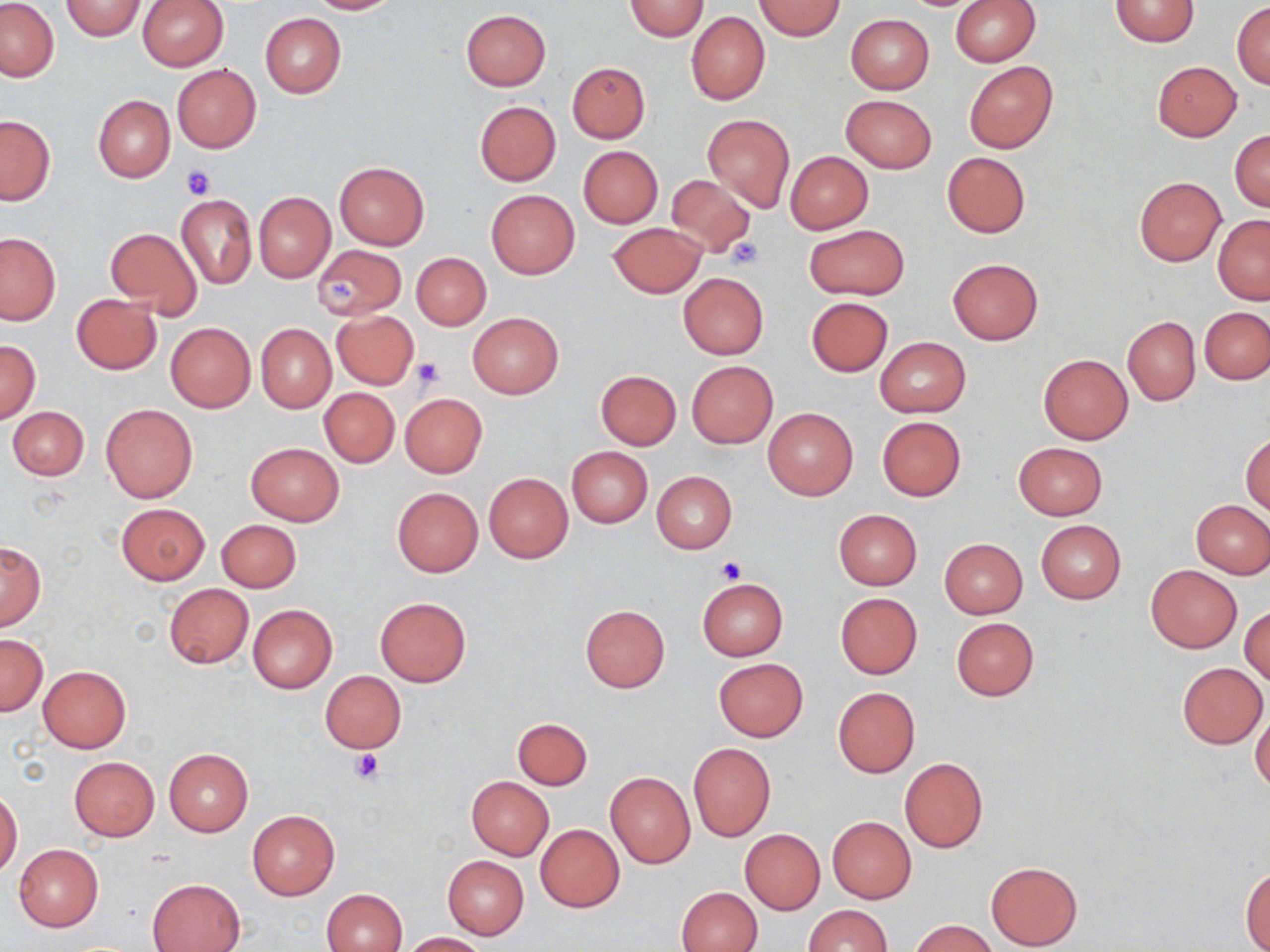

slide_level_diagnosis: no evidence of blood parasites
preparation: thin blood smear
stain: May-Grünwald-Giemsa
platelet_locations: 'approximate bounding boxes as (x1, y1, x2, y2) in pixels: (181, 165, 216, 200), (725, 237, 766, 269), (322, 275, 362, 311), (411, 356, 445, 389), (716, 555, 746, 583), (348, 748, 385, 784)'
uninfected_red_blood_cell_locations: 'approximate bounding boxes as (x1, y1, x2, y2) in pixels: (60, 0, 147, 41), (307, 0, 402, 14), (753, 0, 845, 40), (950, 0, 1040, 65), (1110, 0, 1200, 48), (1, 1, 59, 81), (137, 1, 229, 70), (624, 1, 710, 40), (1232, 2, 1270, 88), (461, 10, 550, 90), (686, 12, 769, 105), (260, 13, 346, 98), (846, 14, 934, 93), (964, 60, 1057, 152), (566, 61, 650, 143), (1151, 61, 1242, 141), (172, 64, 261, 153), (93, 94, 175, 182), (840, 94, 937, 173), (474, 101, 561, 186), (703, 114, 794, 211), (0, 115, 55, 204), (1230, 129, 1270, 212), (579, 146, 663, 227), (785, 151, 872, 234), (942, 151, 1030, 238), (334, 161, 429, 249), (665, 174, 757, 258), (1135, 178, 1225, 265), (486, 189, 579, 278), (254, 192, 335, 283), (175, 194, 257, 289), (1213, 215, 1270, 304), (607, 222, 708, 297), (804, 225, 908, 301), (105, 226, 203, 321), (0, 233, 61, 325), (77, 236, 189, 370), (312, 245, 406, 320), (411, 252, 490, 329), (947, 258, 1044, 346), (678, 272, 769, 360), (70, 294, 162, 374), (806, 297, 893, 376), (1201, 307, 1269, 384), (332, 310, 420, 389), (467, 312, 563, 398), (1122, 316, 1201, 405), (165, 322, 255, 412), (257, 324, 336, 412), (875, 337, 970, 417), (0, 340, 41, 424), (1038, 354, 1132, 444), (687, 361, 777, 448), (596, 370, 681, 450), (319, 387, 399, 468), (399, 393, 488, 478), (101, 403, 198, 503), (8, 406, 89, 480), (763, 407, 858, 501), (877, 416, 966, 500), (1242, 433, 1270, 516), (245, 442, 344, 525), (1013, 442, 1107, 519), (566, 446, 652, 528), (653, 472, 737, 552), (483, 473, 572, 563), (392, 487, 483, 577), (1191, 500, 1270, 578), (115, 503, 209, 584), (833, 509, 922, 589), (216, 519, 301, 592), (1036, 520, 1126, 603), (940, 538, 1028, 619), (0, 543, 45, 630), (1146, 565, 1242, 652), (698, 577, 788, 661), (163, 583, 253, 669), (835, 593, 922, 678), (375, 597, 471, 686), (247, 604, 336, 693), (580, 604, 670, 692), (1240, 604, 1269, 686), (951, 617, 1039, 701), (1, 633, 47, 715), (714, 659, 808, 740), (1176, 661, 1267, 749), (38, 666, 130, 752), (320, 671, 407, 753), (832, 687, 920, 777), (1251, 707, 1270, 794), (512, 717, 592, 790), (688, 743, 775, 841), (164, 749, 253, 836), (69, 757, 159, 840), (899, 757, 988, 853), (605, 772, 696, 868), (466, 776, 554, 860), (0, 790, 22, 878), (246, 810, 339, 900), (828, 816, 916, 903), (535, 824, 625, 912), (740, 829, 824, 914), (13, 844, 104, 932), (441, 855, 529, 939), (986, 861, 1082, 949), (1241, 866, 1270, 950), (148, 878, 245, 951), (675, 886, 762, 952), (323, 888, 408, 952), (803, 904, 893, 951), (911, 920, 995, 952), (401, 932, 486, 951)'
field_of_view: single
modality: optical microscopy
image_size: 1270×952 pixels
magnification: 1000x